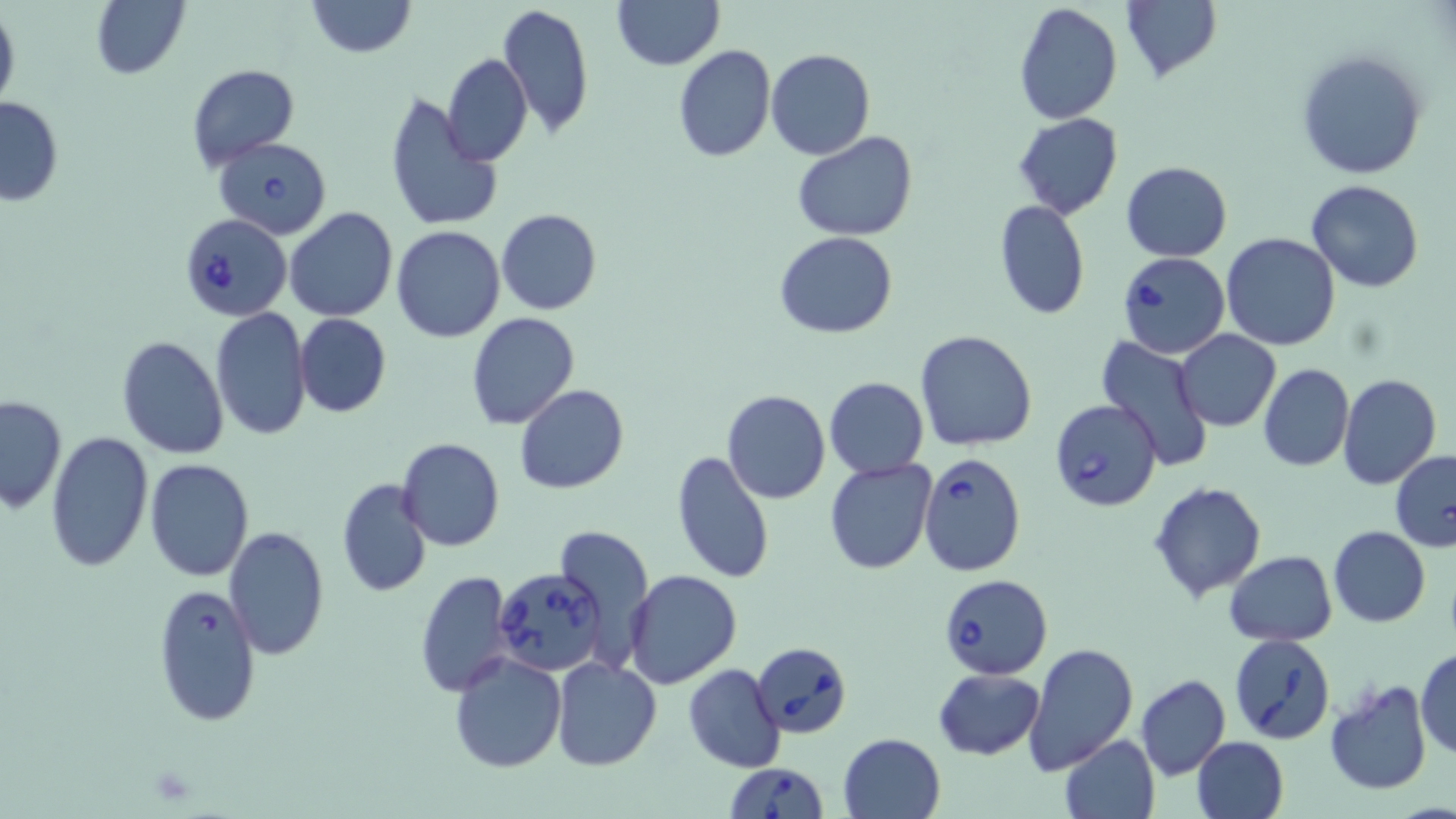

Approximate bounding boxes as [x1, y1, x2, y2] in pixels. Uninfected red blood cell locations: [91, 0, 190, 80], [305, 0, 417, 57], [496, 1, 593, 141], [611, 1, 724, 70], [1120, 1, 1221, 82], [1012, 2, 1122, 125], [0, 6, 20, 119], [673, 45, 776, 163], [1296, 48, 1428, 181], [765, 49, 877, 160], [442, 53, 532, 167], [185, 64, 300, 172], [0, 95, 65, 205], [384, 95, 503, 235], [1013, 112, 1124, 221], [794, 130, 916, 243], [1121, 161, 1232, 261], [1305, 180, 1427, 293], [994, 199, 1090, 320], [282, 207, 398, 323], [497, 207, 602, 314], [390, 226, 506, 343], [774, 232, 898, 339], [1221, 232, 1341, 350], [211, 308, 311, 443], [465, 311, 580, 430], [294, 313, 391, 418], [915, 329, 1038, 450], [1175, 330, 1281, 431], [115, 335, 230, 458], [1097, 337, 1215, 472], [1259, 363, 1353, 471], [1338, 375, 1441, 490], [823, 376, 928, 478], [515, 384, 629, 495], [721, 390, 831, 505], [0, 394, 66, 514], [44, 431, 153, 573], [396, 437, 505, 552], [671, 450, 774, 584], [1390, 450, 1456, 552], [344, 455, 492, 576], [824, 457, 938, 576], [144, 458, 254, 581], [336, 478, 433, 598], [1149, 482, 1267, 601], [554, 525, 655, 666], [1329, 525, 1431, 627], [224, 526, 330, 661], [1224, 549, 1337, 646], [415, 570, 514, 696], [625, 570, 742, 690], [1025, 643, 1138, 773], [1415, 647, 1456, 761], [447, 652, 566, 773], [551, 656, 660, 771], [683, 663, 785, 773], [1384, 664, 1456, 776], [934, 667, 1045, 760], [1135, 674, 1230, 781], [1322, 679, 1433, 797], [838, 732, 946, 819], [1059, 734, 1160, 817], [1191, 736, 1288, 819]. Babesia divergens-infected red blood cell locations: [215, 137, 333, 240], [179, 213, 290, 321], [1117, 252, 1231, 359], [1049, 399, 1161, 512], [918, 452, 1025, 576], [492, 565, 603, 677], [939, 573, 1053, 678], [152, 581, 262, 726], [1229, 635, 1335, 744], [751, 641, 852, 737], [723, 760, 828, 819]. Slide-level diagnosis: Babesia divergens. Image is 1456×819 pixels. Thin blood smear. 1000x magnification. Optical microscopy. May-Grünwald-Giemsa-stained preparation. Single field of view.